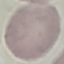

Summary:
  - Malaria status: uninfected
  - Image type: automatically extracted cell patch, resized to 64 × 64 pixels
  - Preparation: thin smear
  - Stain: Giemsa
  - Capture: smartphone through the microscope eyepiece